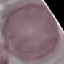 Malaria status: uninfected. Giemsa stain. Photographed with a smartphone camera at the microscope eyepiece. Thin blood film. Cell patch, automatically extracted from a larger field of view and resized to 64 × 64 pixels.